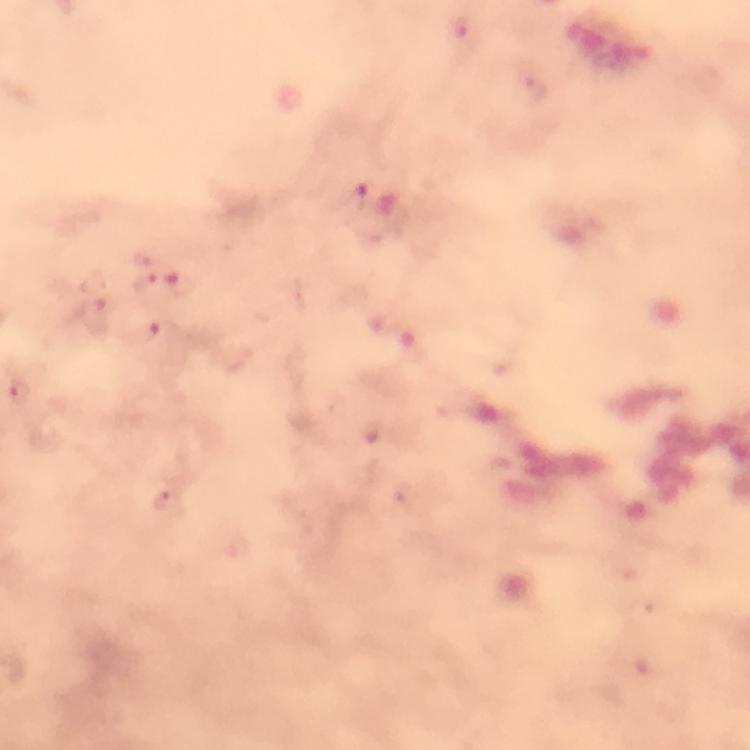
Approximate object centers, in pixels from the top-left corner.
Summary:
  - Malaria parasite locations: (x=461, y=28), (x=536, y=88), (x=352, y=199), (x=142, y=257), (x=180, y=282), (x=147, y=285), (x=94, y=315), (x=144, y=333), (x=20, y=393), (x=373, y=432), (x=168, y=504)
  - Preparation: thick blood film
  - Stain: Giemsa
  - Magnification: 100x
  - Image size: 750×750 pixels
  - Cropped from: one field of view
  - Immersion oil: applied
  - Capture: smartphone photograph through a microscope
  - Context: from a malaria diagnostic workup